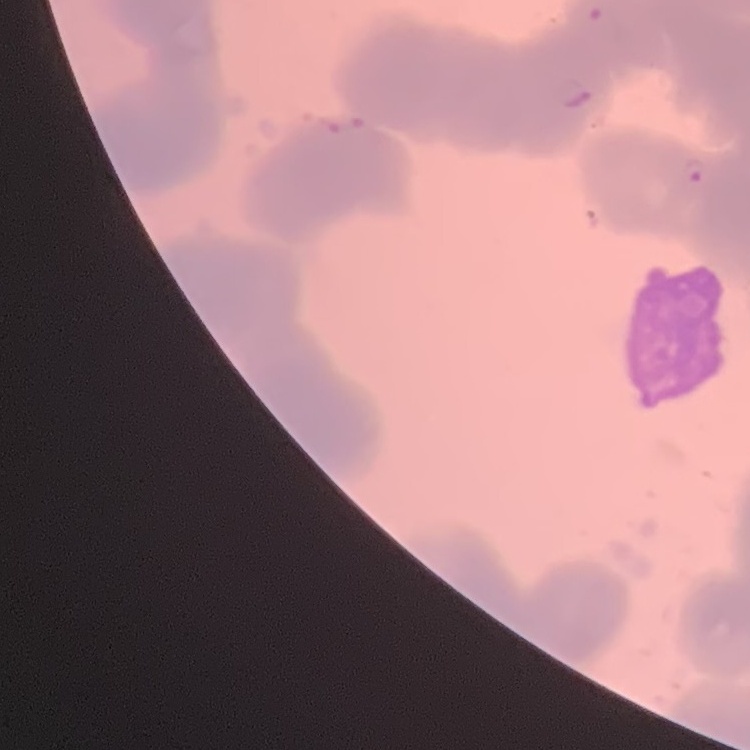

The red blood cells exhibit rouleaux formation. Thin blood film. Stained with either Field's or Giemsa. One tile cut from a larger photomicrograph.